Identify the blood parasite species.
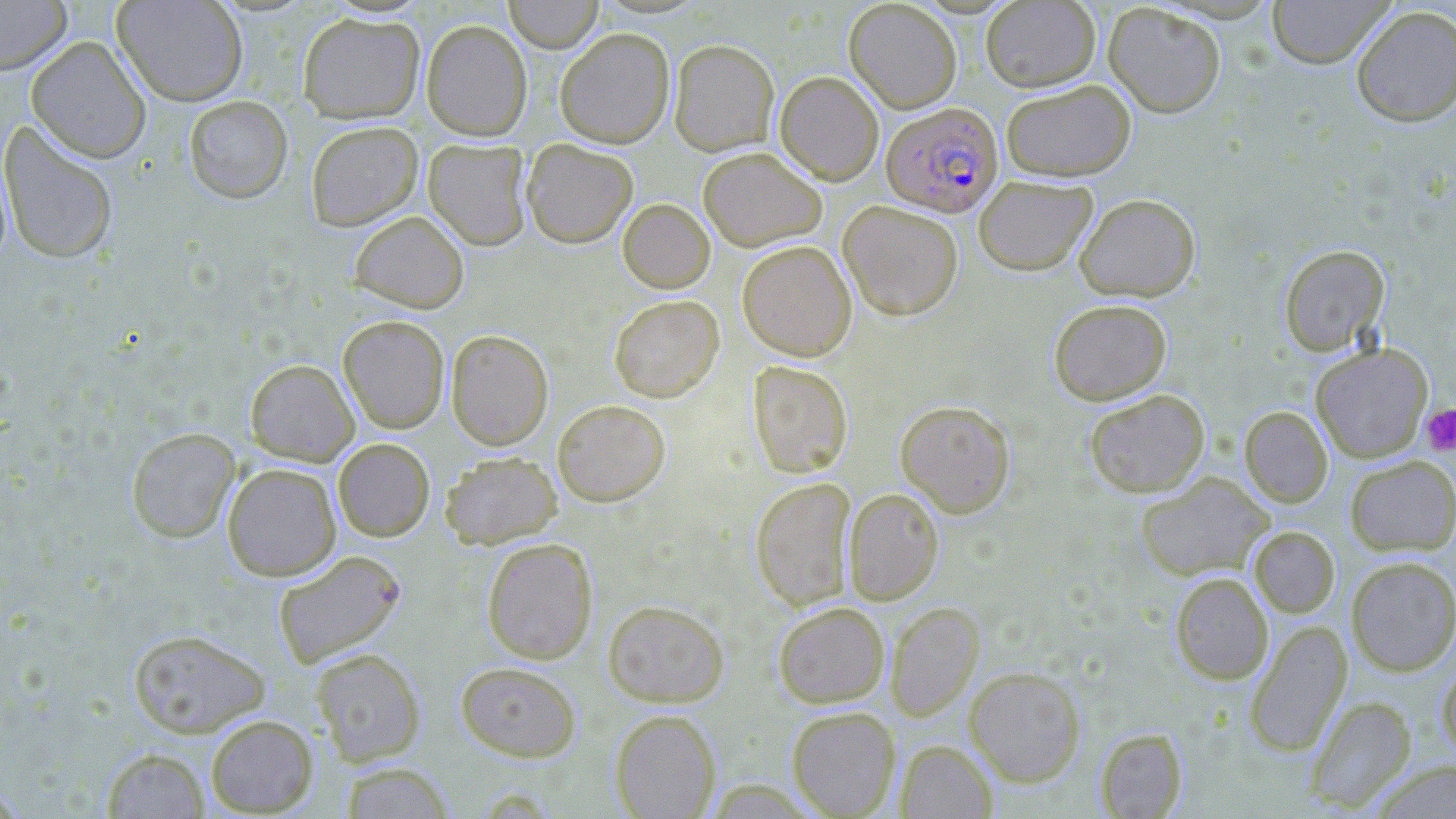
Plasmodium falciparum.

magnification = 1000x
Plasmodium falciparum-infected red blood cell locations = approximate bounding boxes as [x1, y1, x2, y2] in pixels: [881, 102, 1003, 217]
modality = optical microscopy
uninfected red blood cell locations = approximate bounding boxes as [x1, y1, x2, y2] in pixels: [0, 0, 72, 74], [112, 0, 248, 106], [503, 0, 604, 53], [844, 0, 962, 113], [1266, 0, 1394, 69], [980, 1, 1100, 92], [1103, 2, 1226, 118], [1351, 6, 1456, 127], [298, 12, 425, 124], [421, 19, 532, 141], [555, 28, 675, 148], [26, 36, 151, 163], [669, 39, 779, 156], [774, 71, 884, 185], [1001, 78, 1136, 182], [184, 95, 293, 203], [0, 121, 119, 265], [306, 121, 423, 231], [423, 139, 531, 250], [521, 139, 638, 248], [698, 146, 826, 251], [973, 175, 1097, 276], [1074, 193, 1200, 301], [617, 199, 715, 293], [838, 200, 964, 320], [349, 210, 469, 313], [736, 240, 857, 361], [1278, 244, 1389, 356], [609, 294, 724, 402], [1048, 298, 1171, 404], [338, 315, 449, 434], [446, 329, 554, 450], [1310, 343, 1433, 462], [245, 359, 359, 466], [747, 360, 854, 478], [1083, 389, 1210, 497], [552, 399, 670, 506], [895, 399, 1016, 517], [1240, 406, 1332, 508], [126, 426, 241, 542], [333, 438, 434, 541], [440, 451, 561, 548], [1345, 455, 1456, 555], [222, 463, 341, 581], [1136, 471, 1274, 582], [750, 476, 857, 610], [843, 487, 943, 605], [1249, 526, 1339, 618], [481, 537, 598, 664], [273, 550, 406, 668], [1346, 556, 1456, 676], [1170, 572, 1273, 685], [602, 600, 728, 707], [774, 601, 890, 708], [886, 602, 983, 720], [1245, 620, 1352, 756], [127, 628, 270, 738], [311, 648, 426, 764], [1436, 658, 1456, 765], [454, 661, 582, 761], [965, 666, 1086, 786], [1305, 695, 1416, 811], [787, 707, 901, 818], [610, 709, 721, 819], [205, 714, 318, 816], [1096, 728, 1187, 818], [896, 740, 998, 818], [102, 747, 209, 818], [1370, 759, 1456, 818], [339, 761, 455, 818]
platelet locations = approximate bounding boxes as [x1, y1, x2, y2] in pixels: [1420, 404, 1456, 457]
preparation = thin blood smear
image size = 1456×819 pixels
field of view = one of a larger specimen
stain = May-Grünwald-Giemsa